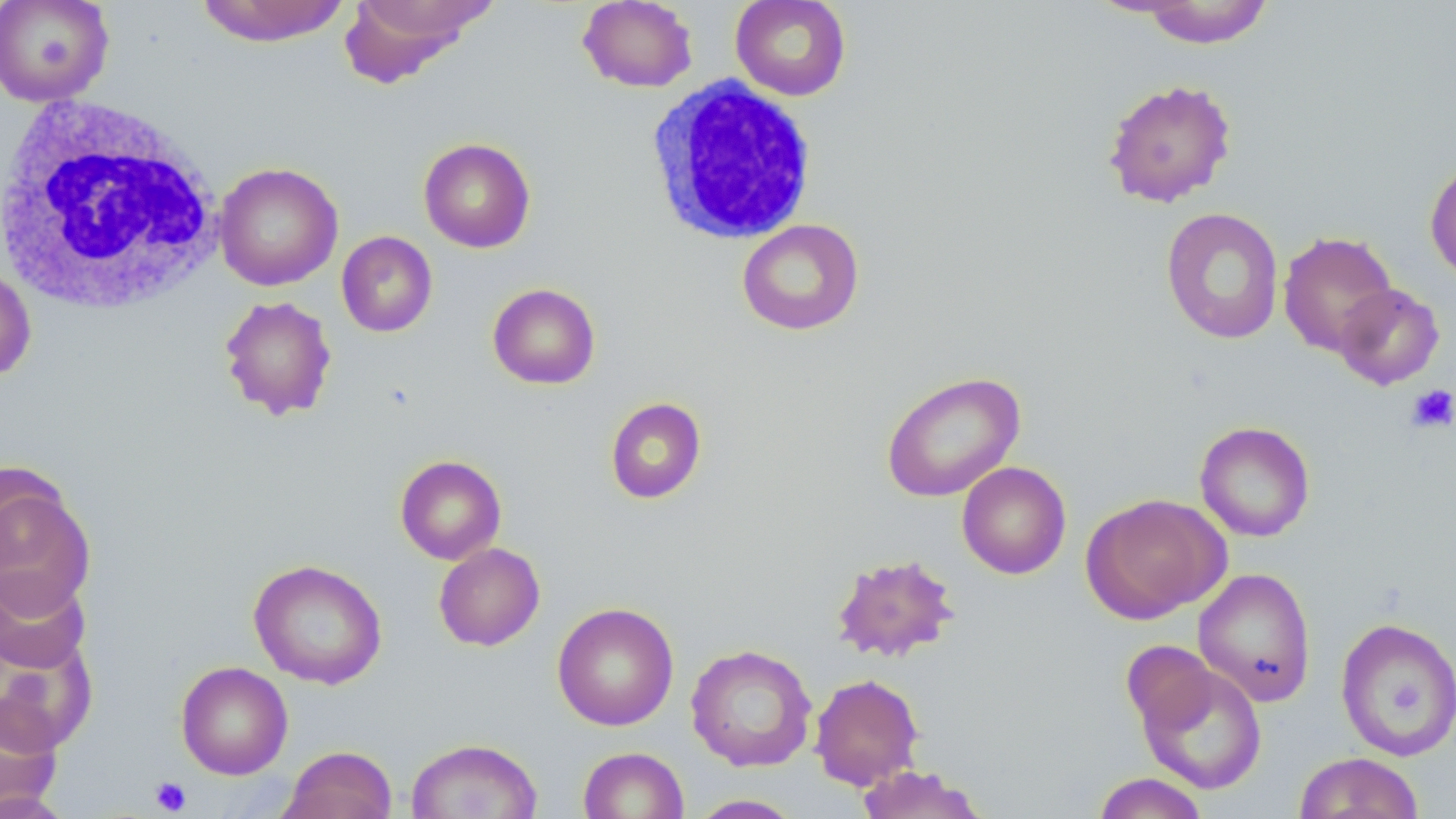
Approximate bounding boxes as (x1, y1, x2, y2) in pixels. Uninfected red blood cell locations: (0, 0, 115, 106), (195, 0, 351, 47), (341, 0, 494, 85), (577, 0, 698, 92), (730, 0, 852, 101), (1137, 1, 1275, 49), (1102, 77, 1238, 208), (418, 137, 535, 253), (1424, 157, 1456, 285), (214, 162, 343, 291), (1160, 207, 1285, 345), (736, 218, 864, 336), (336, 231, 438, 337), (1278, 231, 1398, 357), (0, 265, 37, 382), (487, 282, 601, 389), (1333, 283, 1445, 390), (218, 295, 338, 421), (881, 370, 1025, 502), (604, 397, 707, 504), (1194, 421, 1315, 542), (395, 454, 507, 564), (956, 461, 1071, 579), (0, 472, 95, 618), (1080, 493, 1229, 623), (433, 542, 545, 651), (831, 552, 960, 664), (248, 558, 387, 689), (1193, 567, 1317, 707), (0, 569, 91, 675), (552, 602, 679, 731), (1335, 617, 1456, 759), (0, 636, 97, 752), (1121, 640, 1219, 736), (685, 643, 817, 772), (1135, 660, 1268, 795), (175, 661, 293, 780), (810, 673, 924, 790), (0, 692, 63, 816), (405, 738, 543, 819), (280, 745, 397, 819), (578, 746, 689, 819), (1294, 751, 1426, 819), (855, 765, 989, 818), (1091, 772, 1210, 819), (0, 790, 75, 819), (687, 794, 804, 818). Platelet locations: (1406, 384, 1456, 434), (150, 776, 191, 815). White blood cell locations: (644, 76, 820, 246), (0, 97, 227, 317). Slide-level diagnosis: negative for blood parasites. Image is 1456×819 pixels. Captured at 1000x magnification. May-Grünwald-Giemsa stain. Light microscopy. Thin blood smear. Single field of view.